Give the preparation type.
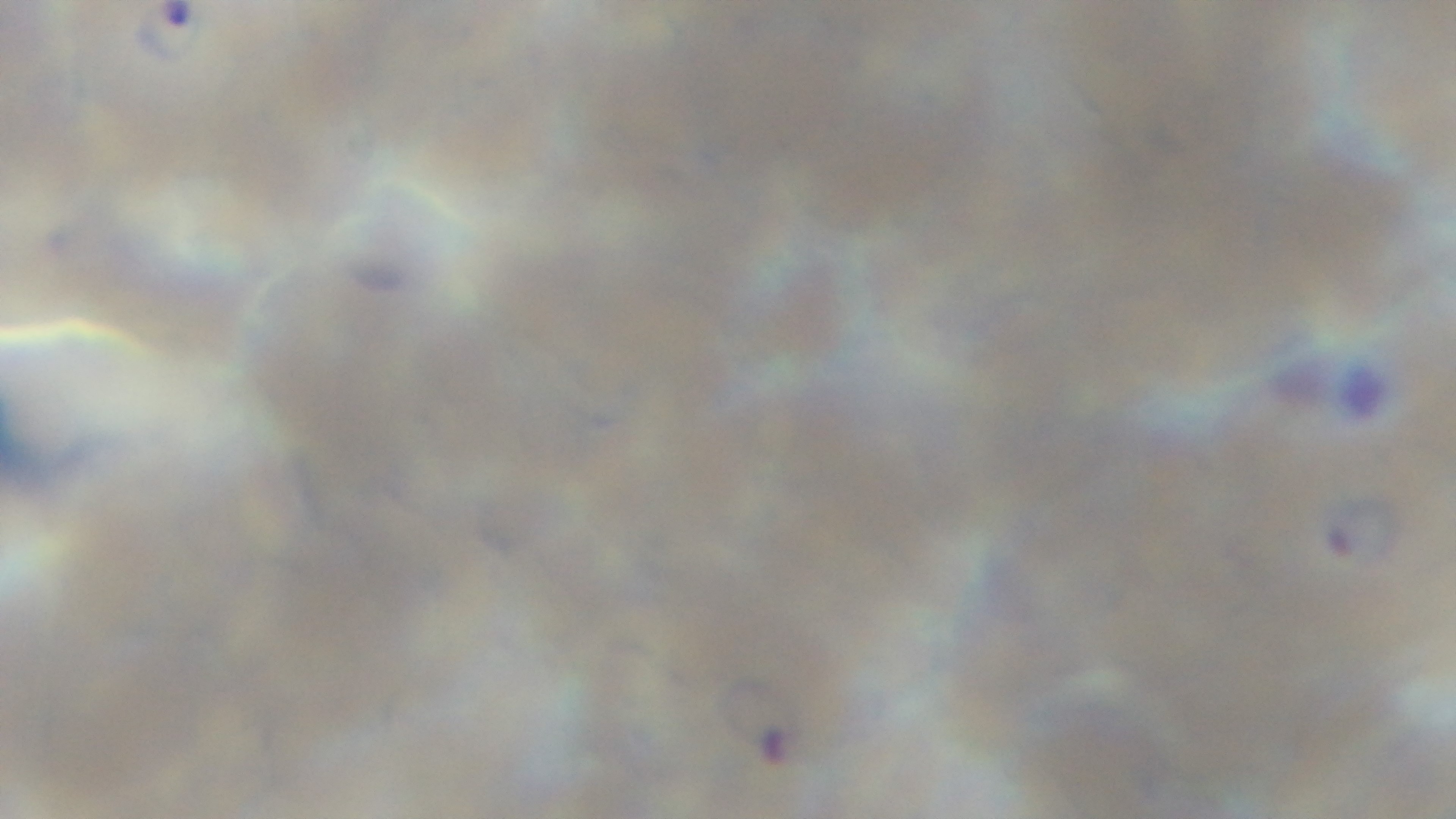
A thin smear.

field of view = one from the slide
modality = light microscopy
capture = mounted 4K digital camera
objective = 100x oil immersion
malaria status = positive
stain = Giemsa